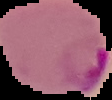
{
  "image_size": "112×100 pixels",
  "result": "malaria parasites identified",
  "image_type": "segmented cell region on a black background",
  "preparation": "thin blood smear"
}